Evaluate for parasitized red blood cells.
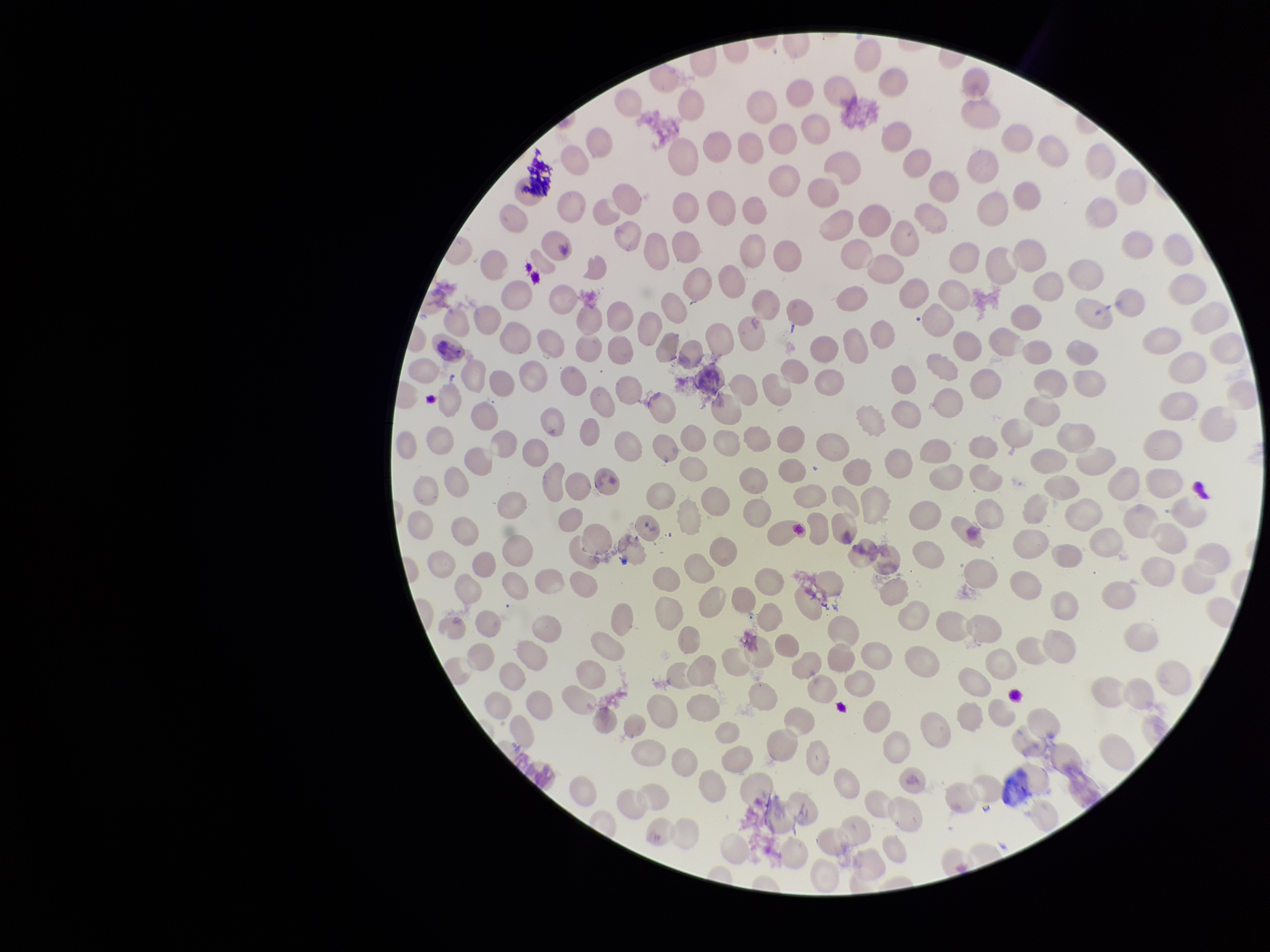
None detected.

Species reported for this patient: Plasmodium vivax. Smartphone photograph taken through the eyepiece of a microscope. Parasitized red blood cell count: 0. Patient malaria status: positive. Giemsa stain. Red blood cell count: 268. Preparation: thin blood smear. Image is 1270×952 pixels. One field from this slide.